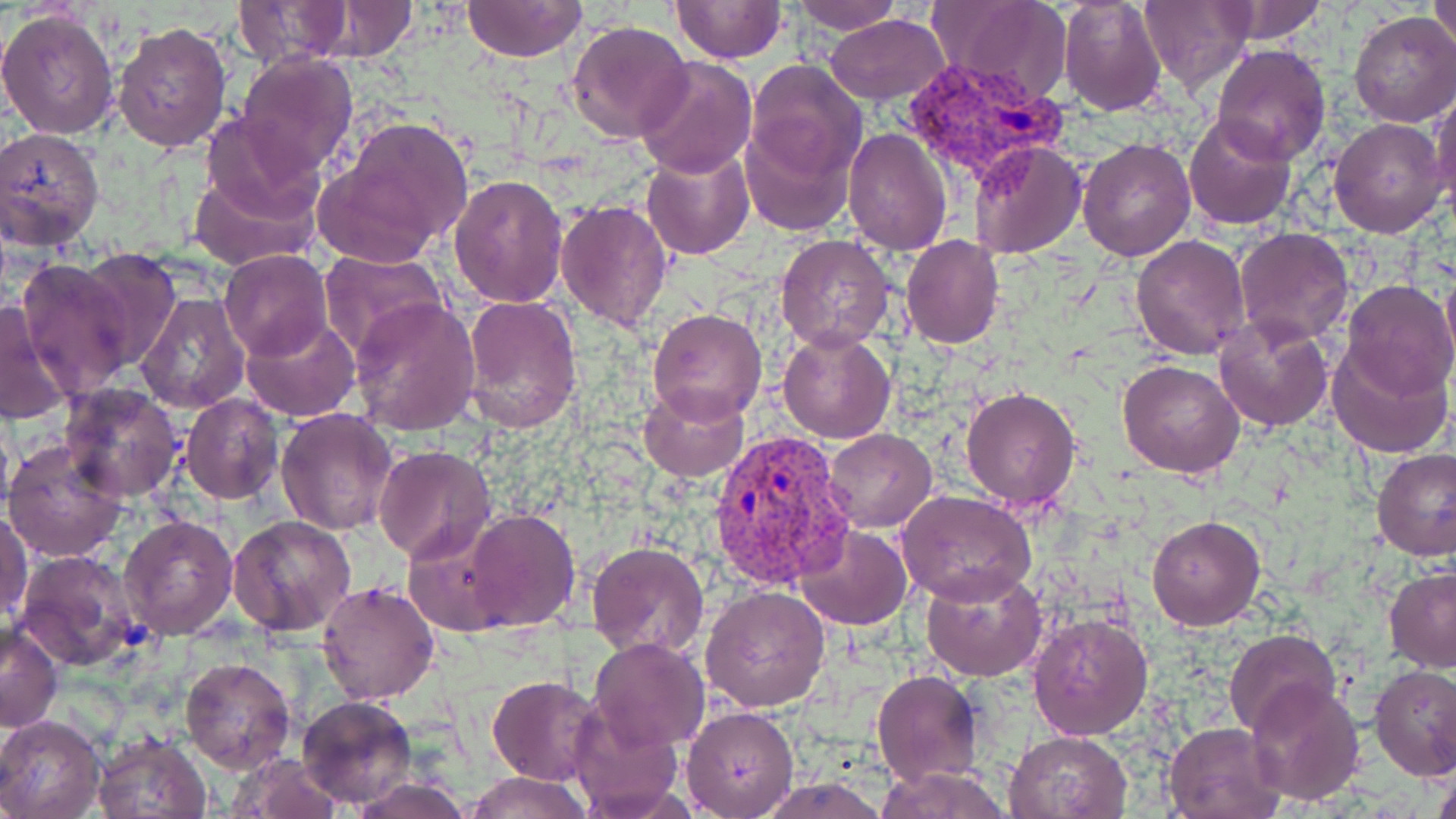

{
  "slide_level_diagnosis": "Plasmodium vivax",
  "preparation": "thin blood smear",
  "image_size": "1456×819 pixels",
  "field_of_view": "single",
  "stain": "May-Grünwald-Giemsa",
  "modality": "optical microscopy",
  "plasmodium_vivax_infected_red_blood_cell_locations": "approximate bounding boxes as named x1/y1/x2/y2 corners in pixels: (x1=906, y1=61, x2=1066, y2=201), (x1=708, y1=429, x2=856, y2=588)",
  "uninfected_red_blood_cell_locations": "approximate bounding boxes as named x1/y1/x2/y2 corners in pixels: (x1=671, y1=0, x2=785, y2=63), (x1=1058, y1=0, x2=1168, y2=116), (x1=231, y1=1, x2=358, y2=67), (x1=459, y1=1, x2=589, y2=62), (x1=786, y1=1, x2=906, y2=35), (x1=929, y1=1, x2=1072, y2=104), (x1=1137, y1=1, x2=1257, y2=93), (x1=1207, y1=1, x2=1328, y2=45), (x1=1427, y1=1, x2=1456, y2=54), (x1=293, y1=3, x2=426, y2=62), (x1=0, y1=8, x2=121, y2=139), (x1=1349, y1=10, x2=1456, y2=128), (x1=824, y1=14, x2=950, y2=104), (x1=565, y1=19, x2=694, y2=144), (x1=113, y1=21, x2=232, y2=153), (x1=1210, y1=45, x2=1330, y2=165), (x1=235, y1=51, x2=360, y2=175), (x1=634, y1=56, x2=758, y2=179), (x1=744, y1=60, x2=868, y2=186), (x1=1431, y1=89, x2=1455, y2=214), (x1=200, y1=109, x2=329, y2=226), (x1=325, y1=114, x2=475, y2=261), (x1=1183, y1=114, x2=1298, y2=231), (x1=1329, y1=118, x2=1447, y2=237), (x1=738, y1=119, x2=855, y2=236), (x1=0, y1=127, x2=106, y2=250), (x1=842, y1=127, x2=953, y2=257), (x1=1077, y1=138, x2=1197, y2=262), (x1=969, y1=139, x2=1087, y2=259), (x1=642, y1=145, x2=754, y2=260), (x1=187, y1=171, x2=317, y2=273), (x1=448, y1=172, x2=570, y2=308), (x1=554, y1=199, x2=673, y2=332), (x1=1234, y1=227, x2=1356, y2=347), (x1=775, y1=234, x2=896, y2=353), (x1=1130, y1=234, x2=1251, y2=360), (x1=901, y1=235, x2=1006, y2=349), (x1=77, y1=248, x2=179, y2=367), (x1=219, y1=250, x2=334, y2=361), (x1=318, y1=251, x2=450, y2=363), (x1=42, y1=253, x2=175, y2=457), (x1=16, y1=258, x2=135, y2=396), (x1=90, y1=258, x2=238, y2=390), (x1=1341, y1=281, x2=1456, y2=400), (x1=134, y1=291, x2=251, y2=412), (x1=461, y1=294, x2=583, y2=435), (x1=349, y1=296, x2=481, y2=435), (x1=0, y1=301, x2=72, y2=426), (x1=647, y1=309, x2=766, y2=425), (x1=239, y1=315, x2=362, y2=421), (x1=1214, y1=316, x2=1333, y2=433), (x1=777, y1=328, x2=896, y2=444), (x1=1328, y1=340, x2=1453, y2=458), (x1=1118, y1=360, x2=1245, y2=478), (x1=58, y1=381, x2=185, y2=503), (x1=638, y1=386, x2=749, y2=482), (x1=960, y1=386, x2=1082, y2=511), (x1=181, y1=394, x2=285, y2=506), (x1=276, y1=408, x2=398, y2=535), (x1=823, y1=428, x2=937, y2=532), (x1=3, y1=438, x2=129, y2=564), (x1=373, y1=445, x2=495, y2=563), (x1=1372, y1=448, x2=1456, y2=562), (x1=899, y1=492, x2=1038, y2=606), (x1=462, y1=509, x2=579, y2=632), (x1=1, y1=511, x2=33, y2=626), (x1=1147, y1=514, x2=1267, y2=630), (x1=117, y1=515, x2=239, y2=639), (x1=228, y1=515, x2=357, y2=637), (x1=794, y1=524, x2=911, y2=630), (x1=586, y1=541, x2=710, y2=660), (x1=18, y1=550, x2=143, y2=672), (x1=919, y1=565, x2=1046, y2=682), (x1=1384, y1=567, x2=1456, y2=672), (x1=316, y1=579, x2=440, y2=705), (x1=702, y1=586, x2=831, y2=712), (x1=1026, y1=611, x2=1152, y2=741), (x1=0, y1=624, x2=64, y2=731), (x1=1224, y1=629, x2=1342, y2=740), (x1=588, y1=637, x2=710, y2=753), (x1=179, y1=656, x2=297, y2=775), (x1=1370, y1=665, x2=1456, y2=781), (x1=871, y1=670, x2=983, y2=788), (x1=487, y1=676, x2=603, y2=785), (x1=1245, y1=681, x2=1366, y2=806), (x1=297, y1=694, x2=416, y2=807), (x1=568, y1=700, x2=683, y2=816), (x1=682, y1=704, x2=799, y2=816), (x1=0, y1=714, x2=105, y2=819), (x1=1163, y1=722, x2=1286, y2=819), (x1=1005, y1=730, x2=1133, y2=818), (x1=91, y1=732, x2=213, y2=818), (x1=225, y1=754, x2=342, y2=818), (x1=875, y1=765, x2=1013, y2=819), (x1=463, y1=771, x2=593, y2=818), (x1=1430, y1=771, x2=1456, y2=819), (x1=347, y1=777, x2=475, y2=818), (x1=757, y1=777, x2=889, y2=817)",
  "magnification": "1000x"
}